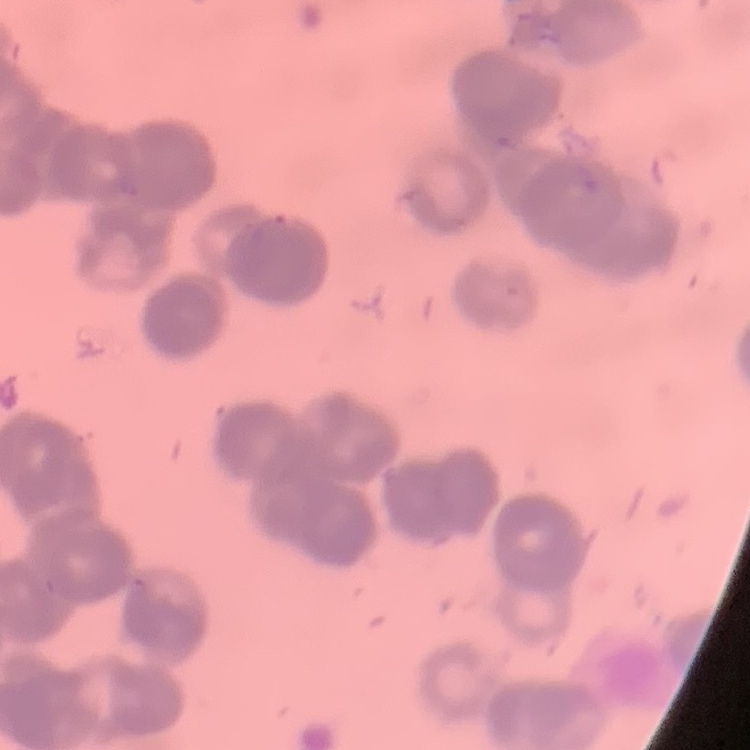 The erythrocytes exhibit rouleaux formation. Square crop of a larger photomicrograph. Field's or Giemsa stain. Thin blood film.